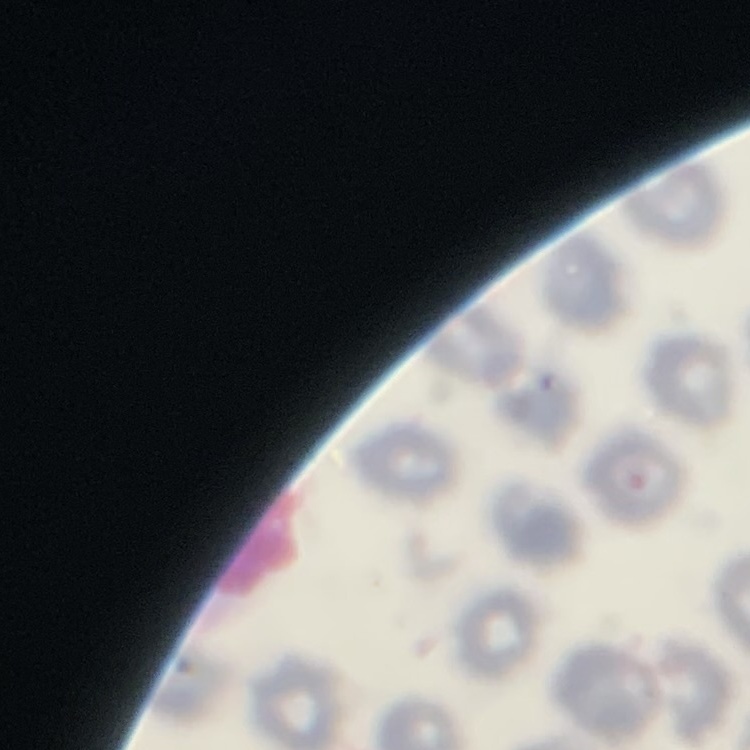

The erythrocytes show no rouleaux formation. Thin peripheral smear. One tile cut from a larger photomicrograph. Field's or Giemsa stain.